State which parasite is depicted.
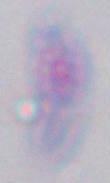
This is Toxoplasma gondii.

modality = photomicrograph
magnification = 1000x